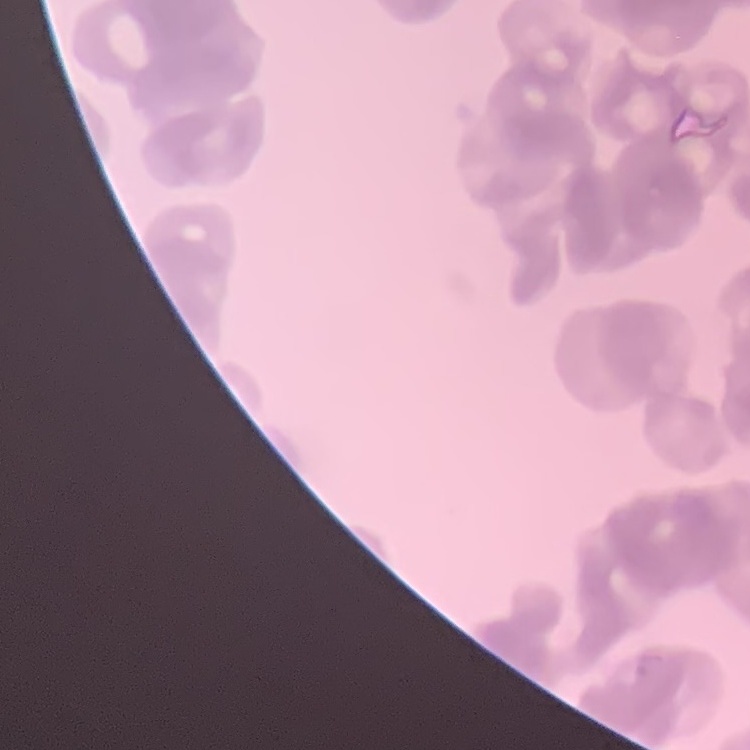
Summary:
  - Erythrocyte morphology: rouleaux formation
  - Preparation: thin blood film
  - Image type: square crop of a larger photomicrograph
  - Stain: Field's or Giemsa